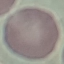

{
  "result": "no malaria parasites detected",
  "preparation": "thin smear",
  "image_type": "cell patch, automatically extracted from a larger field of view and resized to 64 × 64 pixels",
  "capture": "smartphone through the microscope eyepiece",
  "stain": "Giemsa"
}